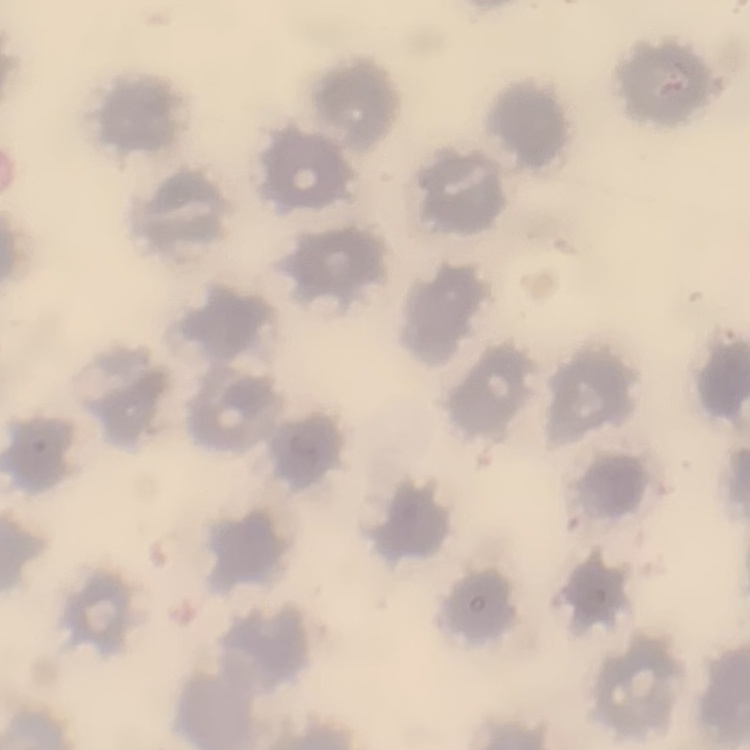 The erythrocytes show no rouleaux formation. One tile cut from a larger photomicrograph. Field's or Giemsa stain. Thin peripheral smear.